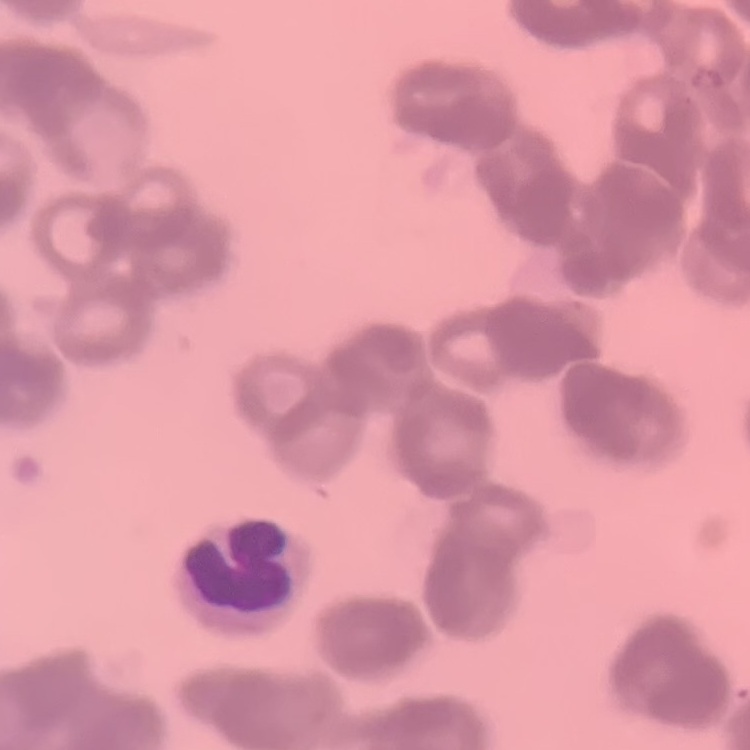

The erythrocytes exhibit rouleaux formation. Square crop of a larger photomicrograph. Thin blood film. Stained with either Field's or Giemsa.